Mark where platelets are.
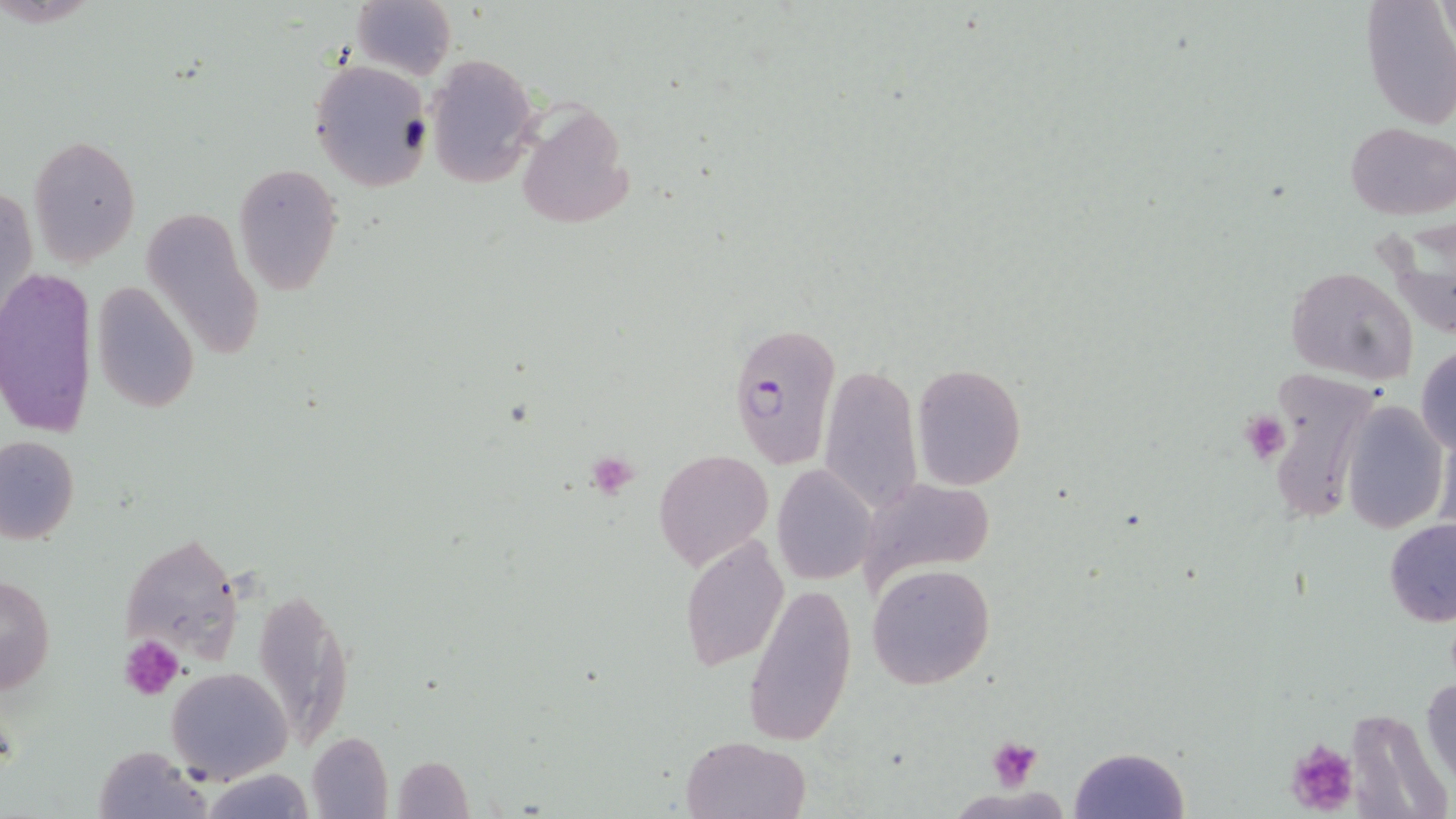
Approximate bounding boxes as (x1,y1)-(x2,y2) corner pairs in pixels.
Platelets: (1237,408)-(1287,464), (584,451)-(639,499), (118,636)-(185,701), (985,736)-(1044,787), (1285,738)-(1360,817).

slide-level diagnosis = Plasmodium falciparum
modality = light microscopy
preparation = thin blood smear
uninfected red blood cell locations = approximate bounding boxes as (x1,y1)-(x2,y2) corner pairs in pixels: (351,0)-(455,79), (1360,0)-(1456,130), (425,54)-(540,186), (308,58)-(434,192), (512,102)-(633,230), (1346,122)-(1455,220), (27,134)-(141,266), (234,165)-(343,296), (2,181)-(37,329), (139,204)-(264,365), (1380,215)-(1456,342), (1287,265)-(1418,384), (0,267)-(97,439), (89,282)-(199,415), (1415,346)-(1456,456), (817,361)-(923,514), (911,363)-(1026,490), (1257,369)-(1380,530), (1340,399)-(1448,533), (0,433)-(80,544), (655,449)-(774,573), (771,466)-(878,585), (859,477)-(992,592), (1384,518)-(1456,627), (118,531)-(244,671), (679,533)-(788,672), (867,563)-(995,689), (0,575)-(57,699), (742,581)-(859,747), (252,585)-(356,752), (164,666)-(292,782), (1423,672)-(1456,791), (307,731)-(393,817), (681,734)-(810,818), (92,744)-(211,818), (1069,747)-(1191,819), (393,756)-(474,817), (199,768)-(317,819)
Plasmodium falciparum-infected red blood cell locations = approximate bounding boxes as (x1,y1)-(x2,y2) corner pairs in pixels: (727,319)-(841,471)
magnification = 1000x
field of view = single
stain = May-Grünwald-Giemsa
image size = 1456×819 pixels